Report the malaria status of this cell.
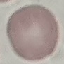

It is uninfected.

Thin smear of blood. Photographed with a smartphone camera at the microscope eyepiece. Automatically extracted cell patch, resized to 64 × 64 pixels. Giemsa stain.